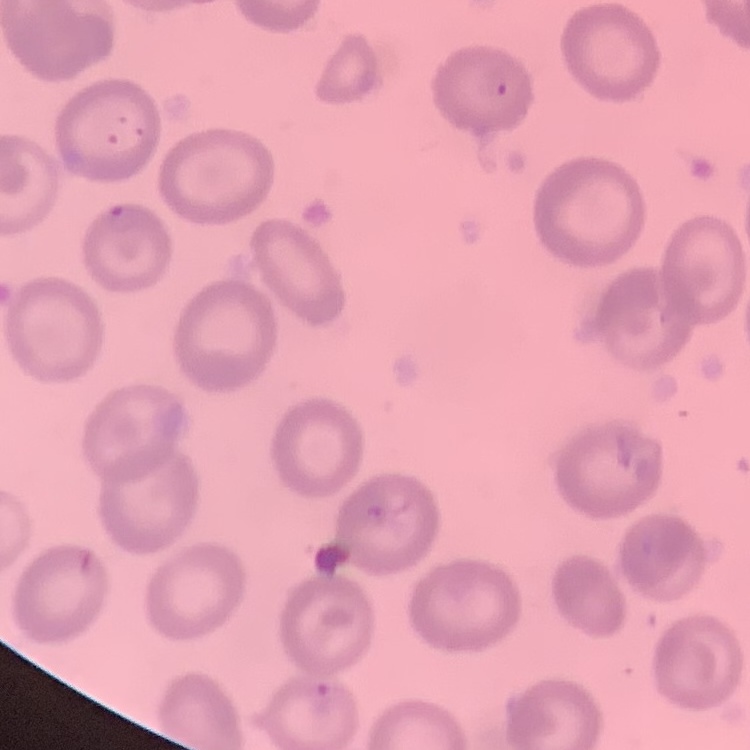
Summary:
  - Red blood cell morphology: no rouleaux formation
  - Image type: square crop of a larger photomicrograph
  - Preparation: thin peripheral smear
  - Stain: Field's or Giemsa